Classify this cell by malaria status.
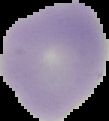
It is uninfected.

image type = segmented cell region with the area outside set to black
preparation = thin blood smear
image size = 109×121 pixels